Assess this cell for malaria.
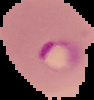
It is parasitized.

Summary:
  - Preparation: thin blood film
  - Image size: 94×100 pixels
  - Image type: segmented cell region with the area outside set to black